Evaluate for Plasmodium parasites.
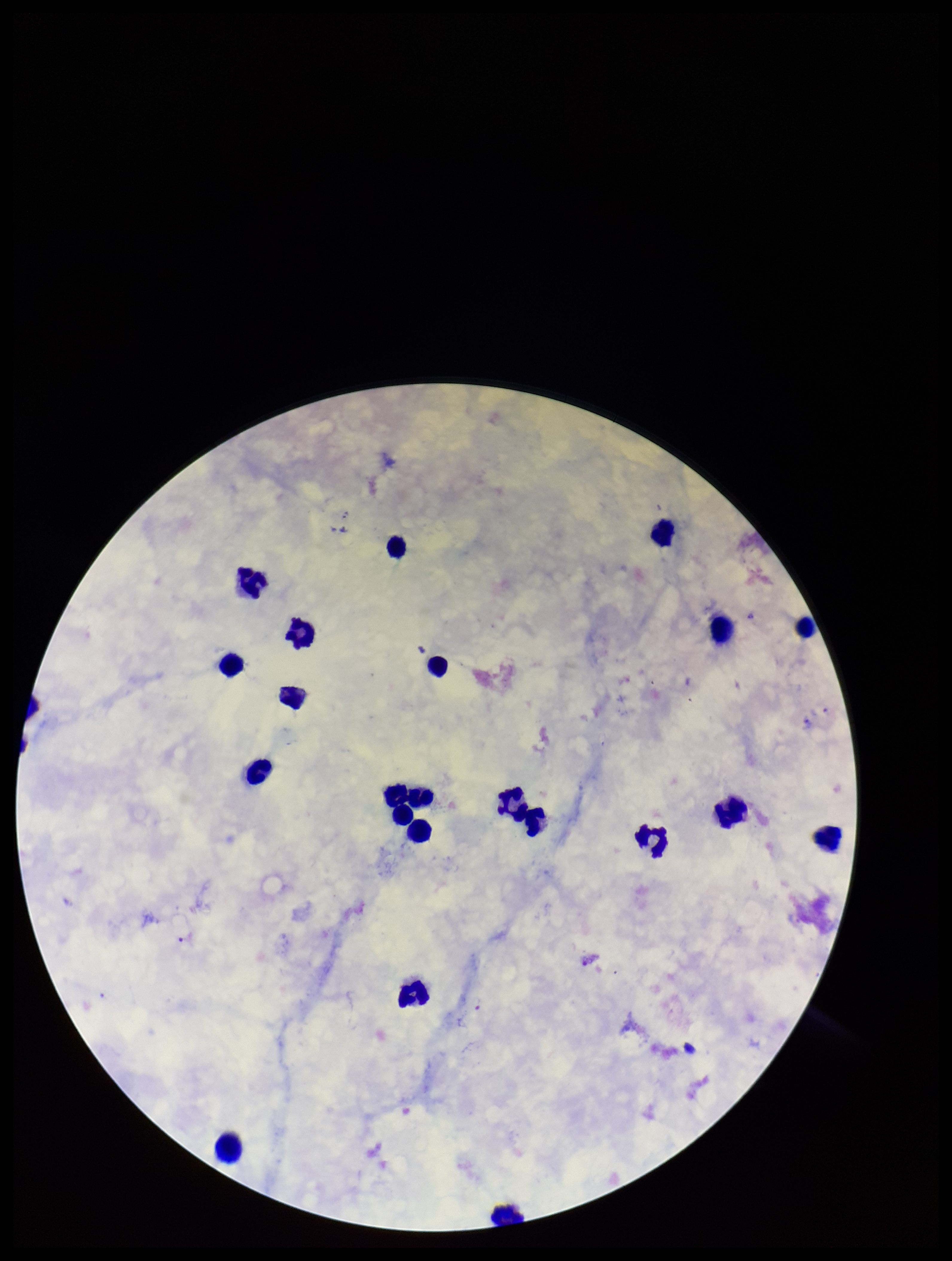

Detected.

field of view = one from this slide
capture = smartphone photograph through the microscope eyepiece
patient malaria status = positive
leukocyte count = 22
stain = Giemsa
parasite count = 1
species reported for this patient = Plasmodium falciparum
preparation = thick blood smear
image size = 952×1261 pixels